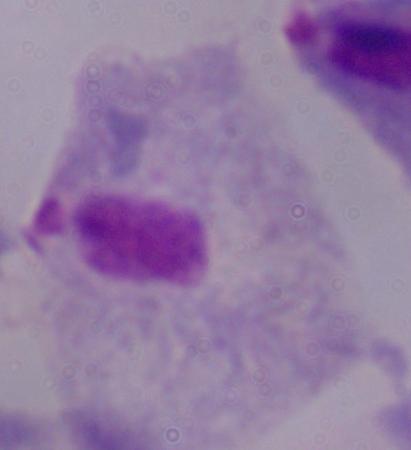

{
  "magnification": "1000x",
  "identification": "trichomonad",
  "modality": "photomicrograph"
}